Report the malaria status of this cell.
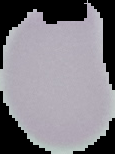

Uninfected.

preparation: thin blood smear
image_type: segmented cell region with the area outside set to black
image_size: 115×154 pixels